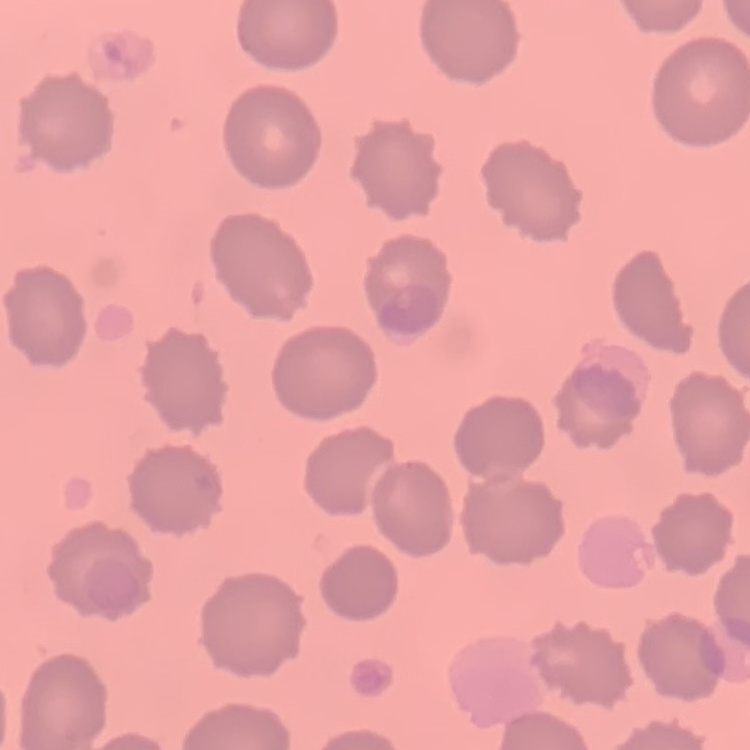
red blood cell morphology = no rouleaux formation
stain = Field's or Giemsa
image type = one tile cut from a larger photomicrograph
preparation = thin peripheral smear